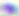

Summary:
  - Identification: Toxoplasma gondii
  - Modality: photomicrograph
  - Magnification: 400x